Report the malaria status of this cell.
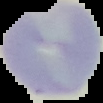
It is uninfected.

{
  "preparation": "thin blood film",
  "image_size": "103×103 pixels",
  "image_type": "segmented cell region on a black background"
}